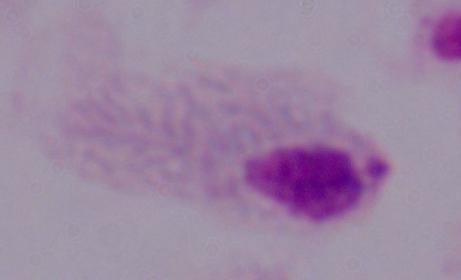

Photomicrograph. Captured at 1000x magnification. A trichomonad is seen.